Assess this cell for malaria.
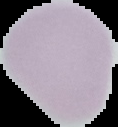

It is uninfected.

{
  "image_type": "cell region segmented out of the field of view; surrounding area masked to black",
  "preparation": "thin blood smear",
  "image_size": "118×127 pixels"
}